Report the malaria status of this cell.
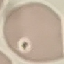
It is uninfected.

stain = Giemsa
capture = smartphone through the microscope eyepiece
preparation = thin blood film
image type = automatically extracted cell patch, resized to 64 × 64 pixels